Give the position of every malaria parasite.
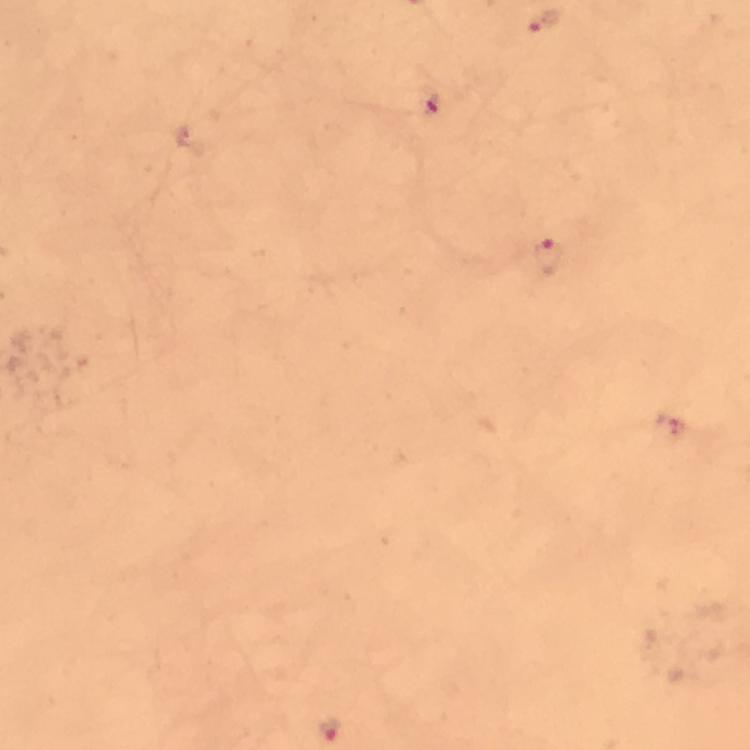
Approximate centers as [x, y] in pixels.
Malaria parasites: [545, 22], [431, 108], [547, 258], [671, 423], [330, 728].

{
  "preparation": "thick blood smear",
  "image_size": "750×750 pixels",
  "context": "from a diagnostic examination for malaria",
  "capture": "smartphone camera through the microscope",
  "stain": "Giemsa",
  "immersion_oil": "used",
  "cropped_from": "a single field of view",
  "magnification": "100x"
}